Comment on the morphology of the erythrocytes.
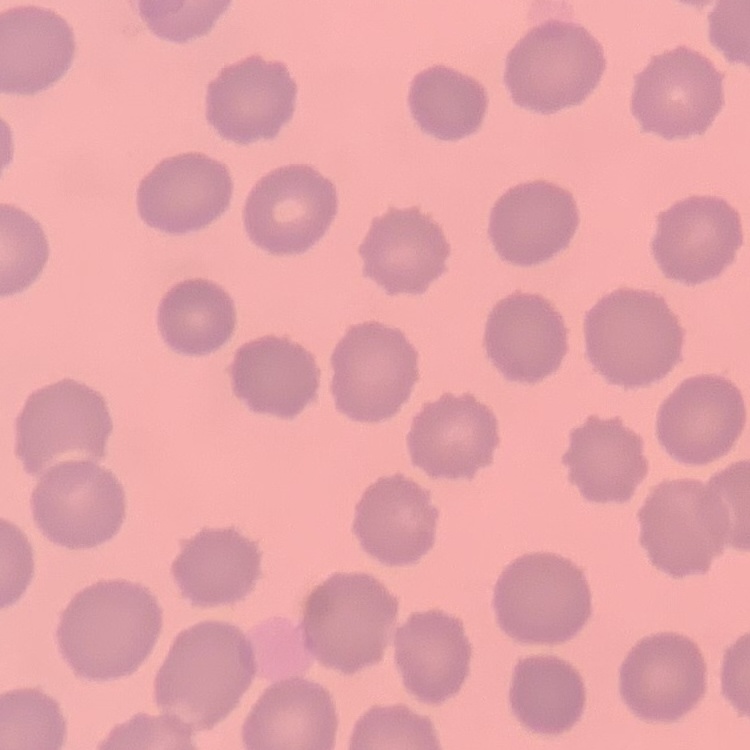
They show no rouleaux formation.

Summary:
  - Image type: one tile cut from a larger photomicrograph
  - Stain: Field's or Giemsa
  - Preparation: thin peripheral smear